Outline each blood parasite and name the species.
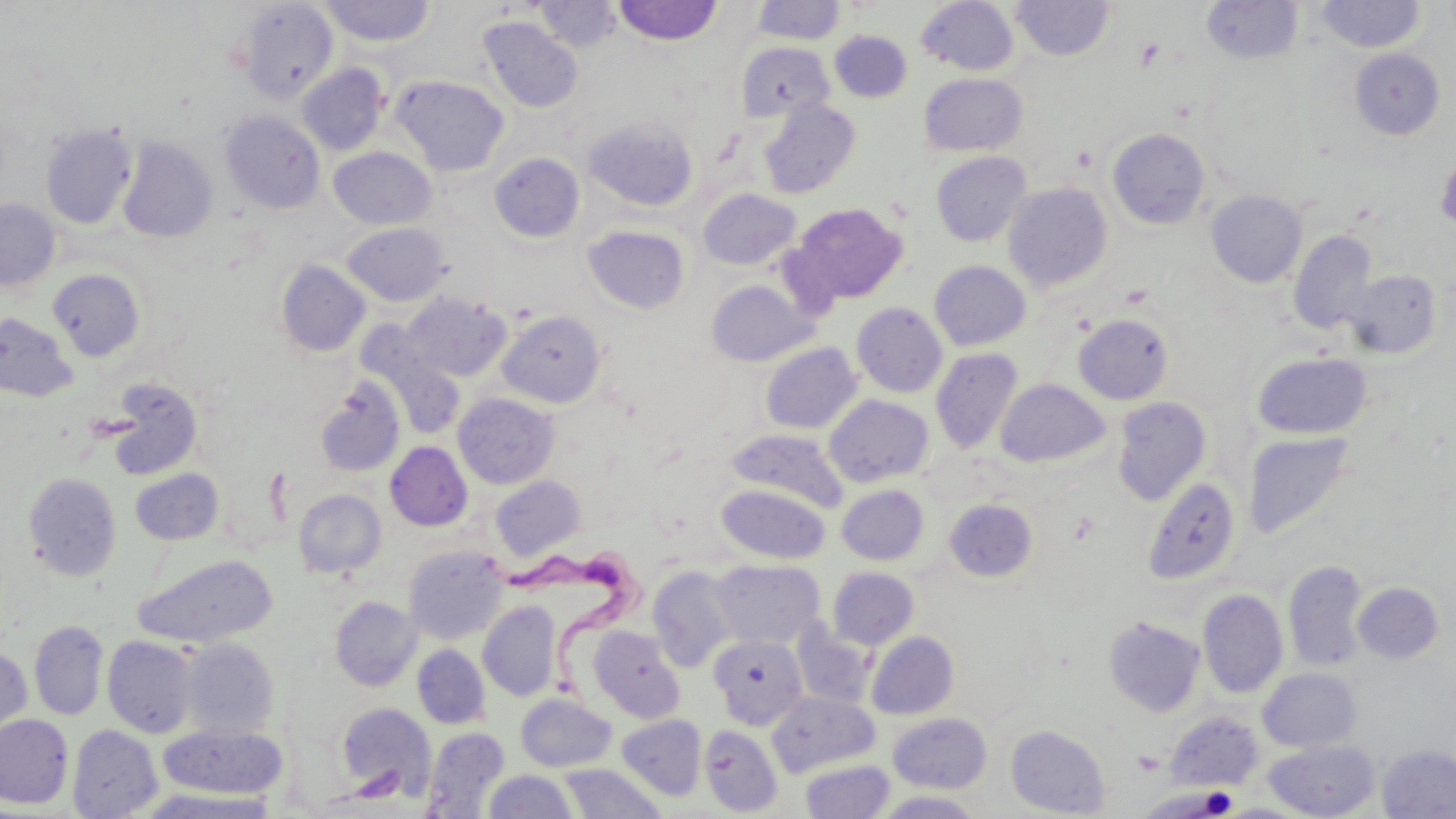
Approximate bounding boxes as named x1/y1/x2/y2 corners in pixels.
Trypanosoma brucei: (x1=483, y1=538, x2=652, y2=706).
No Plasmodium falciparum, Plasmodium ovale, Plasmodium malariae, Plasmodium vivax, or Babesia divergens observed.

Platelet locations: (x1=1198, y1=786, x2=1238, y2=816), (x1=1156, y1=787, x2=1233, y2=817). Uninfected red blood cell locations: (x1=319, y1=1, x2=435, y2=46), (x1=531, y1=1, x2=623, y2=51), (x1=613, y1=1, x2=723, y2=45), (x1=751, y1=1, x2=846, y2=45), (x1=916, y1=1, x2=1020, y2=75), (x1=1010, y1=1, x2=1116, y2=61), (x1=1201, y1=1, x2=1303, y2=64), (x1=1316, y1=1, x2=1426, y2=53), (x1=235, y1=2, x2=339, y2=103), (x1=477, y1=16, x2=584, y2=114), (x1=829, y1=30, x2=912, y2=102), (x1=737, y1=41, x2=834, y2=122), (x1=1349, y1=48, x2=1445, y2=140), (x1=296, y1=63, x2=390, y2=155), (x1=919, y1=73, x2=1028, y2=156), (x1=391, y1=75, x2=509, y2=176), (x1=759, y1=99, x2=861, y2=199), (x1=221, y1=111, x2=324, y2=214), (x1=584, y1=115, x2=699, y2=211), (x1=40, y1=125, x2=137, y2=228), (x1=1107, y1=128, x2=1210, y2=229), (x1=117, y1=136, x2=218, y2=243), (x1=329, y1=147, x2=436, y2=229), (x1=931, y1=151, x2=1031, y2=247), (x1=489, y1=152, x2=584, y2=243), (x1=1003, y1=182, x2=1113, y2=292), (x1=698, y1=189, x2=801, y2=270), (x1=1206, y1=190, x2=1307, y2=287), (x1=0, y1=199, x2=60, y2=290), (x1=789, y1=203, x2=908, y2=305), (x1=342, y1=222, x2=451, y2=305), (x1=582, y1=225, x2=690, y2=314), (x1=1289, y1=229, x2=1379, y2=334), (x1=276, y1=260, x2=370, y2=356), (x1=929, y1=260, x2=1030, y2=350), (x1=48, y1=268, x2=145, y2=361), (x1=1341, y1=269, x2=1442, y2=358), (x1=706, y1=279, x2=817, y2=366), (x1=402, y1=291, x2=511, y2=382), (x1=852, y1=302, x2=948, y2=397), (x1=497, y1=309, x2=606, y2=408), (x1=0, y1=312, x2=78, y2=402), (x1=1074, y1=314, x2=1174, y2=404), (x1=367, y1=342, x2=466, y2=440), (x1=760, y1=342, x2=862, y2=434), (x1=930, y1=347, x2=1023, y2=454), (x1=1252, y1=352, x2=1372, y2=439), (x1=315, y1=377, x2=405, y2=477), (x1=104, y1=378, x2=204, y2=480), (x1=995, y1=378, x2=1110, y2=467), (x1=453, y1=393, x2=559, y2=488), (x1=824, y1=394, x2=934, y2=486), (x1=1112, y1=396, x2=1211, y2=505), (x1=726, y1=428, x2=847, y2=512), (x1=1243, y1=431, x2=1356, y2=541), (x1=385, y1=441, x2=472, y2=531), (x1=130, y1=468, x2=224, y2=545), (x1=23, y1=472, x2=122, y2=581), (x1=491, y1=475, x2=586, y2=560), (x1=1141, y1=476, x2=1241, y2=585), (x1=716, y1=484, x2=830, y2=563), (x1=837, y1=484, x2=928, y2=565), (x1=293, y1=489, x2=386, y2=577), (x1=944, y1=498, x2=1037, y2=581), (x1=403, y1=545, x2=508, y2=644), (x1=133, y1=555, x2=278, y2=648), (x1=709, y1=559, x2=824, y2=648), (x1=1283, y1=560, x2=1369, y2=671), (x1=647, y1=565, x2=738, y2=672), (x1=828, y1=567, x2=919, y2=649), (x1=1352, y1=582, x2=1443, y2=663), (x1=1198, y1=589, x2=1288, y2=698), (x1=330, y1=596, x2=421, y2=691), (x1=478, y1=601, x2=561, y2=701), (x1=1103, y1=617, x2=1205, y2=716), (x1=29, y1=620, x2=108, y2=721), (x1=791, y1=620, x2=875, y2=709), (x1=588, y1=625, x2=685, y2=722), (x1=867, y1=632, x2=959, y2=719), (x1=709, y1=634, x2=807, y2=729), (x1=103, y1=636, x2=198, y2=738), (x1=179, y1=637, x2=280, y2=738), (x1=412, y1=644, x2=490, y2=729), (x1=0, y1=645, x2=33, y2=744), (x1=1258, y1=667, x2=1362, y2=752), (x1=767, y1=691, x2=879, y2=776), (x1=515, y1=693, x2=616, y2=772), (x1=336, y1=702, x2=436, y2=802), (x1=1166, y1=711, x2=1263, y2=790), (x1=887, y1=712, x2=993, y2=793), (x1=0, y1=713, x2=73, y2=808), (x1=617, y1=714, x2=707, y2=800), (x1=68, y1=724, x2=163, y2=818), (x1=159, y1=724, x2=287, y2=798), (x1=1006, y1=724, x2=1110, y2=817), (x1=700, y1=725, x2=783, y2=816), (x1=422, y1=727, x2=510, y2=817), (x1=1263, y1=739, x2=1381, y2=819), (x1=1377, y1=744, x2=1456, y2=818), (x1=800, y1=759, x2=894, y2=819), (x1=559, y1=764, x2=665, y2=818), (x1=484, y1=770, x2=578, y2=818), (x1=1137, y1=786, x2=1236, y2=817), (x1=133, y1=788, x2=281, y2=818), (x1=875, y1=791, x2=987, y2=818). Slide-level diagnosis: Trypanosoma brucei. Thin blood smear. Image is 1456×819 pixels. Optical microscopy. 1000x magnification. One field of a larger specimen. May-Grünwald-Giemsa stain.